Identify the parasite.
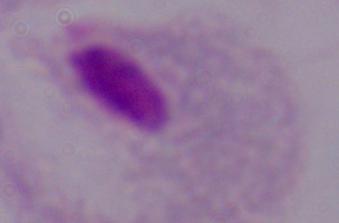

A trichomonad.

Photomicrograph. 1000x magnification.